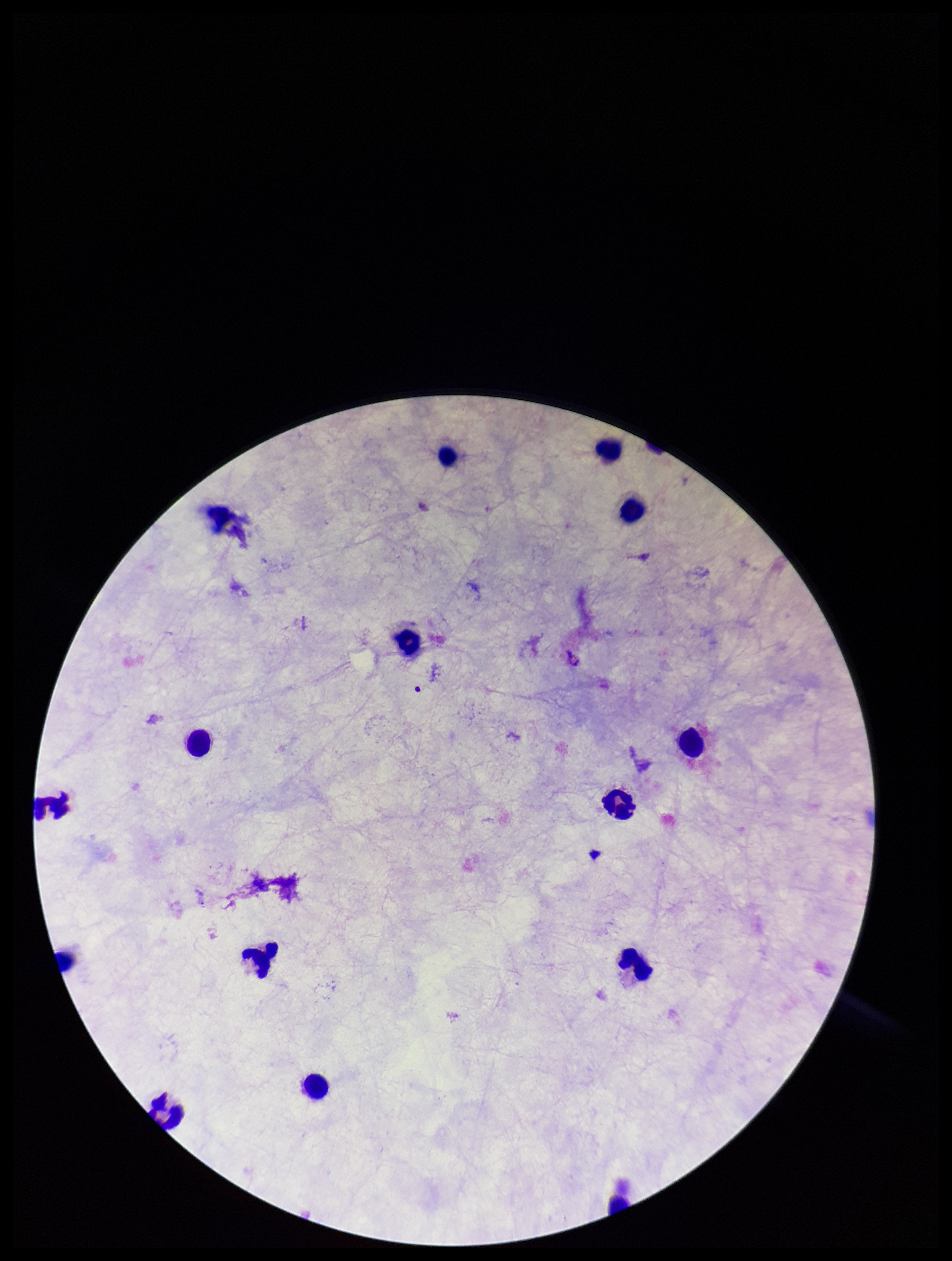 Plasmodium parasites: none detected. Parasite count: 0. Single field of view. Image is 952×1261 pixels. Photographed through the microscope eyepiece with a smartphone camera. Preparation: thick. Leukocyte count: 14. Stained with Giemsa. Patient malaria status: negative.